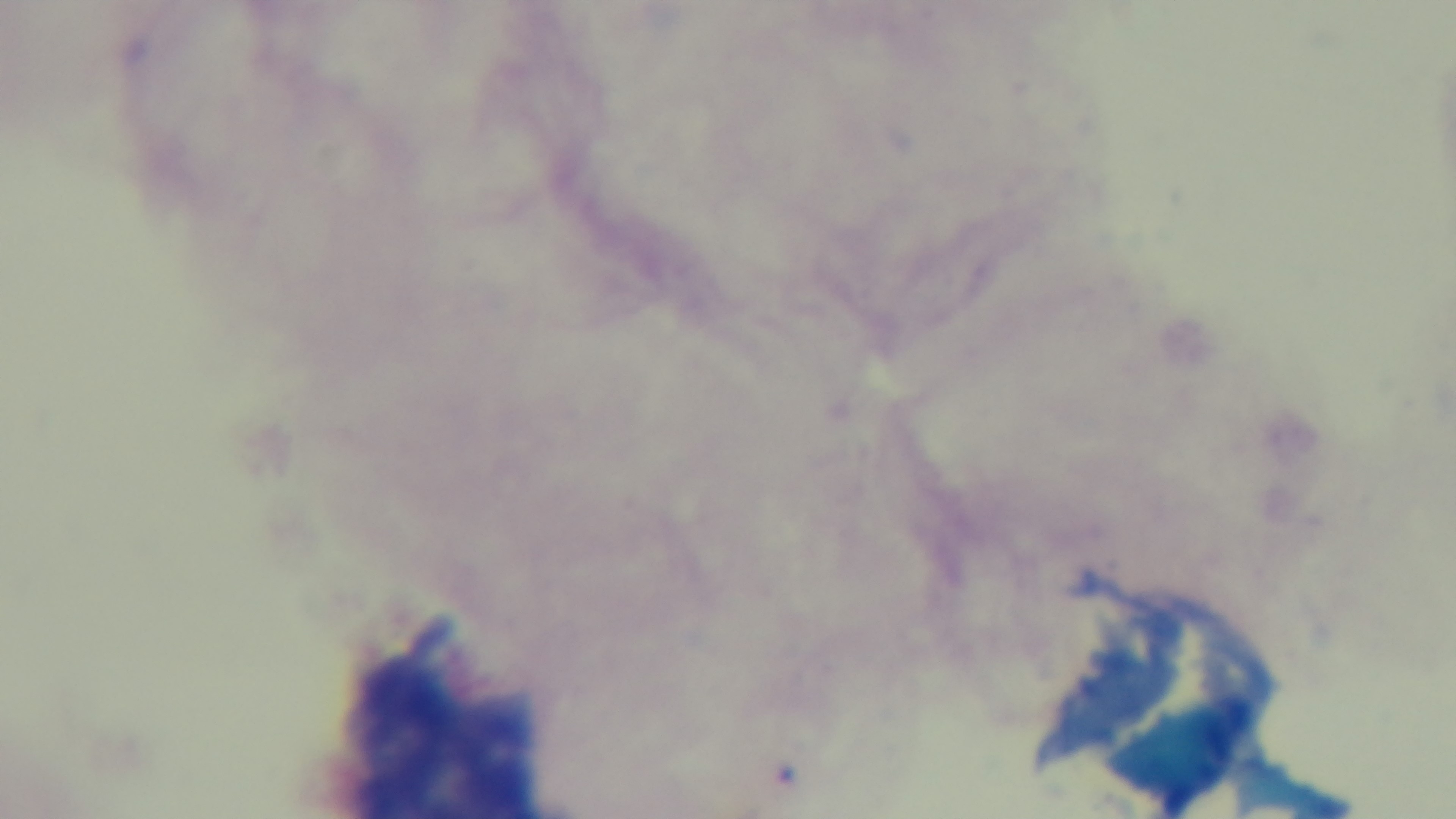
Giemsa stain. 100x oil-immersion objective. One field from the slide. Preparation: thick. Malaria status: uninfected. Mounted 4K digital camera. Light microscopy.